Assess this cell for malaria.
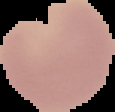

It is uninfected.

Cell region segmented out of the field of view; the surrounding area is masked to black. From a thin blood smear. Image is 115×112 pixels.